Give the preparation type.
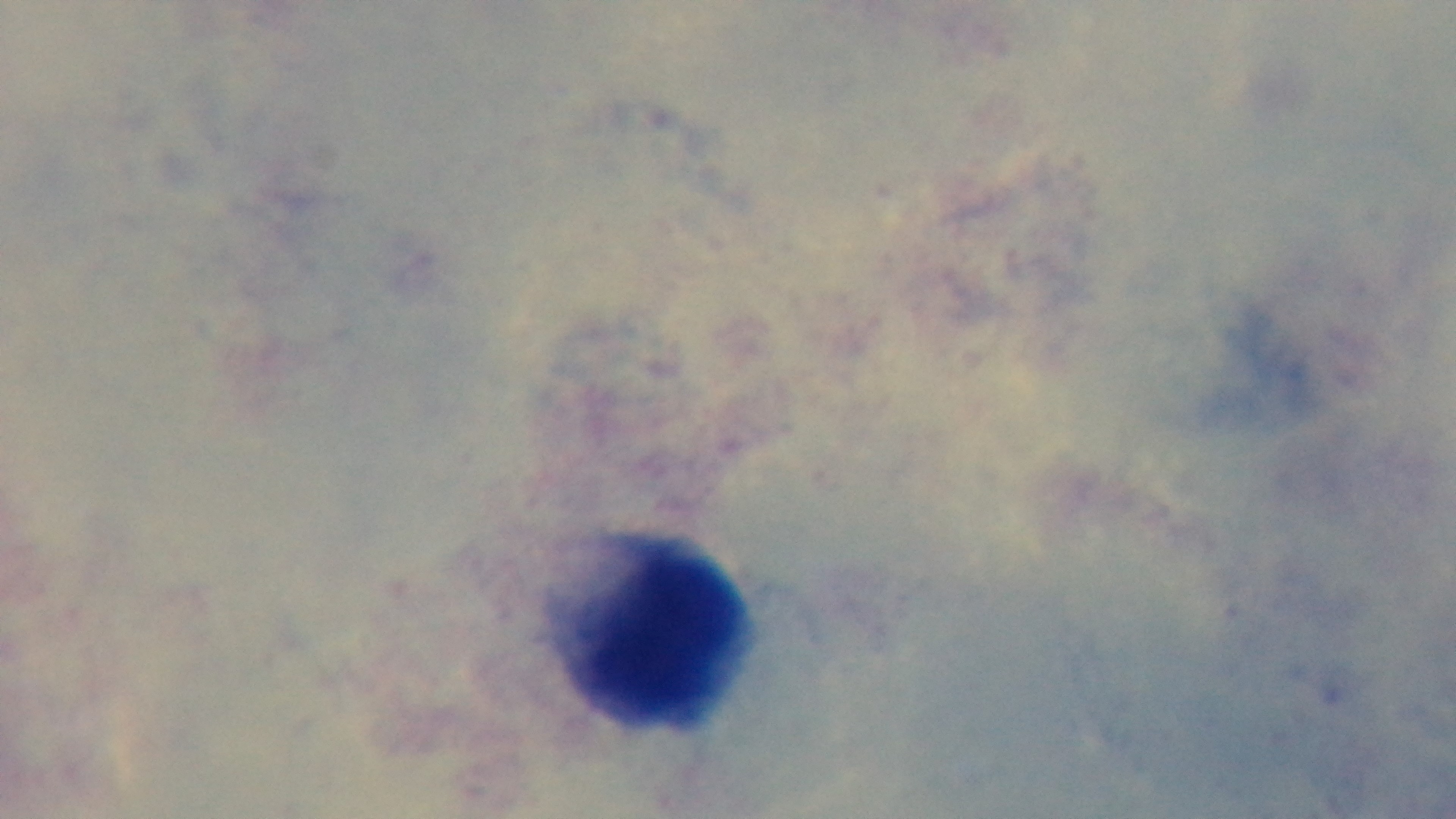
A thick smear.

stain = Giemsa
modality = light microscopy
malaria status = uninfected
field of view = single
capture = mounted 4K digital camera
objective = 100x oil immersion